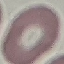

Summary:
  - Malaria status: uninfected
  - Preparation: thin smear
  - Capture: smartphone through the microscope eyepiece
  - Stain: Giemsa
  - Image type: automatically extracted cell patch, resized to 64 × 64 pixels